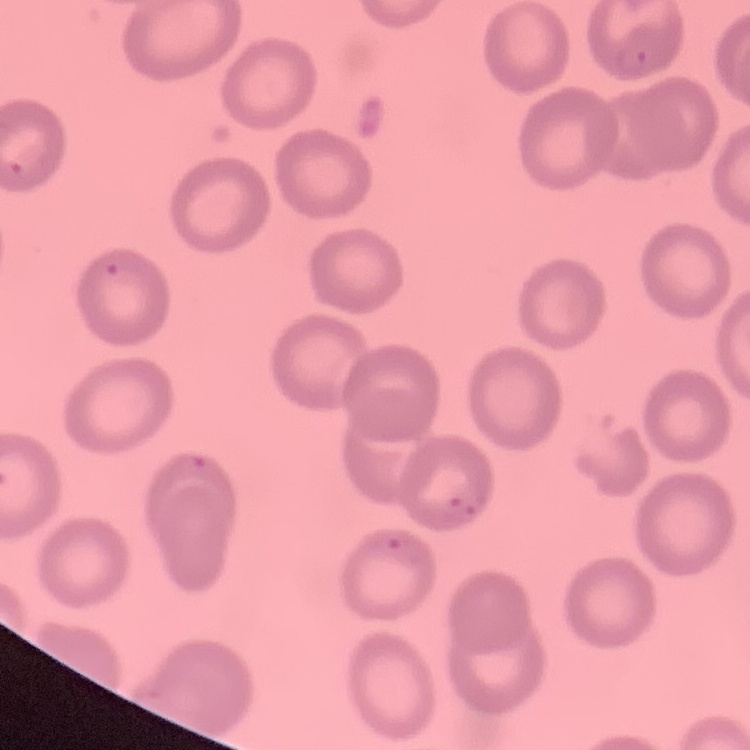
The red blood cells exhibit no rouleaux formation. Stained with either Field's or Giemsa. Thin peripheral smear. One tile cut from a larger photomicrograph.